Locate every Plasmodium malariae-infected red blood cell.
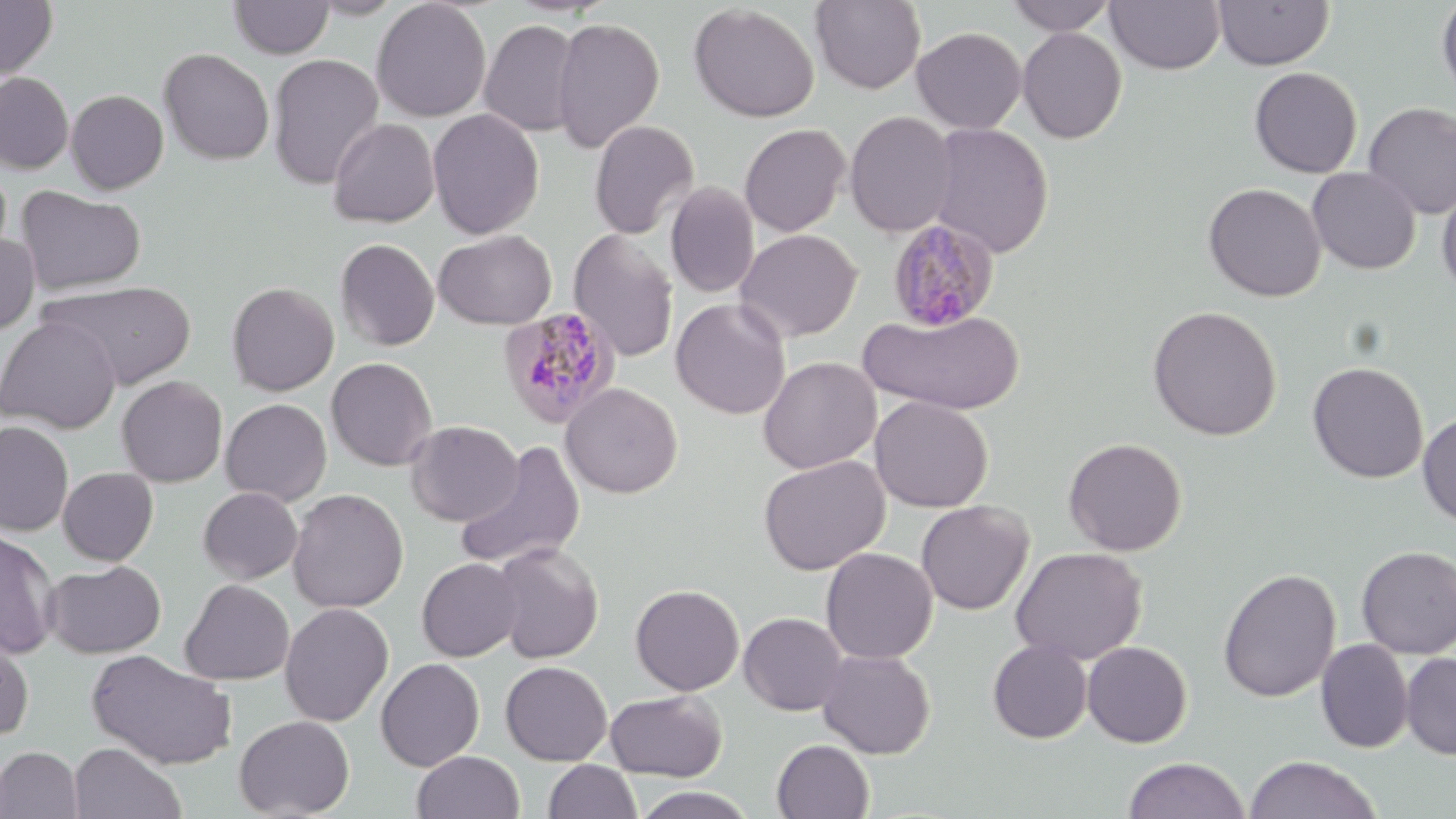

Approximate bounding boxes as named x1/y1/x2/y2 corners in pixels.
Plasmodium malariae-infected red blood cells: (x1=886, y1=218, x2=1000, y2=331), (x1=497, y1=306, x2=622, y2=429).

{
  "slide_level_diagnosis": "Plasmodium malariae",
  "stain": "May-Grünwald-Giemsa",
  "preparation": "thin blood smear",
  "magnification": "1000x",
  "image_size": "1456×819 pixels",
  "modality": "optical microscopy",
  "uninfected_red_blood_cell_locations": "approximate bounding boxes as named x1/y1/x2/y2 corners in pixels: (x1=0, y1=0, x2=58, y2=80), (x1=228, y1=0, x2=335, y2=59), (x1=307, y1=0, x2=408, y2=19), (x1=371, y1=0, x2=492, y2=122), (x1=1005, y1=0, x2=1119, y2=35), (x1=1213, y1=0, x2=1334, y2=70), (x1=1436, y1=0, x2=1456, y2=103), (x1=809, y1=1, x2=926, y2=94), (x1=1106, y1=1, x2=1226, y2=74), (x1=689, y1=4, x2=819, y2=122), (x1=551, y1=16, x2=665, y2=152), (x1=479, y1=19, x2=582, y2=137), (x1=912, y1=27, x2=1027, y2=133), (x1=1017, y1=27, x2=1127, y2=143), (x1=158, y1=48, x2=274, y2=165), (x1=266, y1=53, x2=384, y2=189), (x1=1249, y1=67, x2=1363, y2=178), (x1=0, y1=72, x2=74, y2=173), (x1=66, y1=89, x2=168, y2=194), (x1=1362, y1=102, x2=1456, y2=219), (x1=427, y1=109, x2=544, y2=239), (x1=844, y1=110, x2=957, y2=237), (x1=328, y1=117, x2=440, y2=228), (x1=588, y1=119, x2=700, y2=239), (x1=739, y1=123, x2=850, y2=237), (x1=927, y1=123, x2=1053, y2=258), (x1=1307, y1=166, x2=1421, y2=274), (x1=665, y1=181, x2=760, y2=298), (x1=1203, y1=182, x2=1326, y2=302), (x1=1437, y1=182, x2=1456, y2=298), (x1=15, y1=185, x2=146, y2=295), (x1=567, y1=228, x2=679, y2=363), (x1=434, y1=229, x2=556, y2=329), (x1=736, y1=229, x2=862, y2=342), (x1=0, y1=232, x2=40, y2=336), (x1=335, y1=238, x2=439, y2=351), (x1=40, y1=280, x2=196, y2=389), (x1=226, y1=281, x2=339, y2=395), (x1=670, y1=298, x2=791, y2=419), (x1=1147, y1=305, x2=1282, y2=440), (x1=860, y1=307, x2=1024, y2=415), (x1=0, y1=315, x2=120, y2=434), (x1=758, y1=356, x2=881, y2=474), (x1=326, y1=357, x2=438, y2=471), (x1=1307, y1=361, x2=1429, y2=484), (x1=116, y1=375, x2=227, y2=488), (x1=561, y1=382, x2=683, y2=498), (x1=869, y1=396, x2=993, y2=512), (x1=220, y1=398, x2=332, y2=506), (x1=1417, y1=411, x2=1456, y2=527), (x1=406, y1=420, x2=522, y2=526), (x1=0, y1=422, x2=74, y2=536), (x1=1063, y1=437, x2=1187, y2=556), (x1=454, y1=439, x2=587, y2=572), (x1=758, y1=455, x2=889, y2=575), (x1=58, y1=467, x2=158, y2=565), (x1=197, y1=487, x2=303, y2=584), (x1=287, y1=488, x2=409, y2=613), (x1=916, y1=500, x2=1034, y2=615), (x1=0, y1=528, x2=60, y2=659), (x1=490, y1=542, x2=604, y2=663), (x1=1356, y1=545, x2=1456, y2=659), (x1=1010, y1=546, x2=1147, y2=665), (x1=820, y1=547, x2=938, y2=664), (x1=417, y1=557, x2=523, y2=662), (x1=44, y1=560, x2=165, y2=658), (x1=1217, y1=567, x2=1342, y2=703), (x1=180, y1=579, x2=294, y2=685), (x1=630, y1=584, x2=744, y2=695), (x1=279, y1=602, x2=394, y2=727), (x1=739, y1=612, x2=848, y2=715), (x1=0, y1=627, x2=34, y2=741), (x1=988, y1=639, x2=1093, y2=743), (x1=1316, y1=639, x2=1413, y2=753), (x1=1082, y1=641, x2=1192, y2=748), (x1=85, y1=649, x2=239, y2=770), (x1=817, y1=649, x2=936, y2=759), (x1=1401, y1=652, x2=1456, y2=760), (x1=376, y1=657, x2=485, y2=771), (x1=500, y1=661, x2=612, y2=766), (x1=606, y1=690, x2=727, y2=781), (x1=234, y1=715, x2=355, y2=818), (x1=771, y1=739, x2=874, y2=819), (x1=68, y1=742, x2=187, y2=819), (x1=0, y1=746, x2=83, y2=819), (x1=412, y1=751, x2=525, y2=819), (x1=1244, y1=754, x2=1381, y2=818), (x1=1123, y1=756, x2=1250, y2=818), (x1=543, y1=760, x2=642, y2=819), (x1=631, y1=787, x2=759, y2=819)",
  "field_of_view": "one of a larger specimen"
}